Assess the morphology of the erythrocytes.
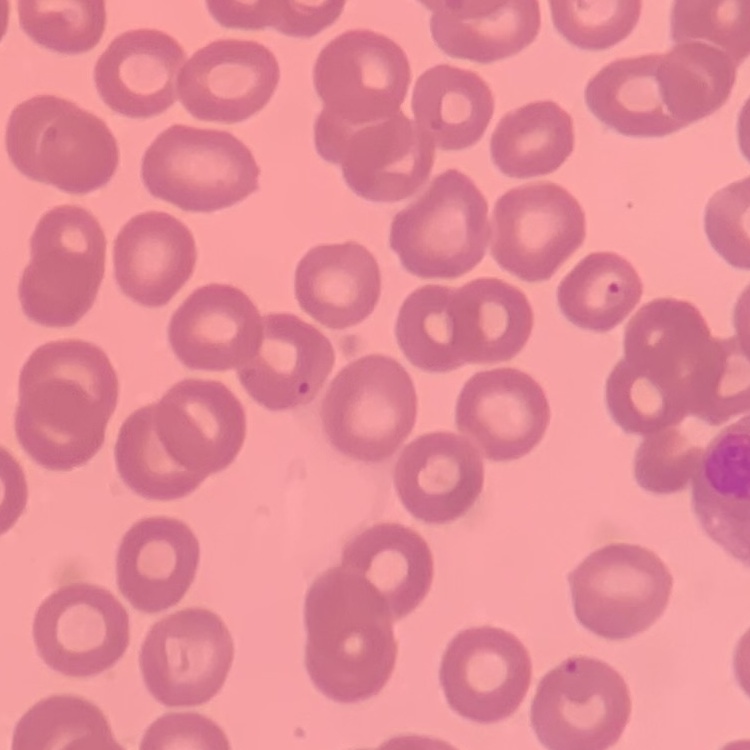

They show no rouleaux formation.

Field's or Giemsa stain. One tile cut from a larger photomicrograph. Thin peripheral smear.